State which parasite is depicted.
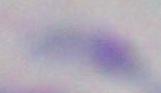

This is Toxoplasma gondii.

modality = micrograph
magnification = 1000x